Identify the cell.
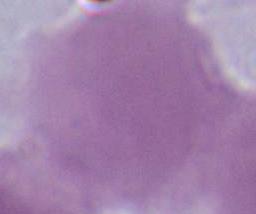

An erythrocyte.

Photomicrograph. 1000x magnification.